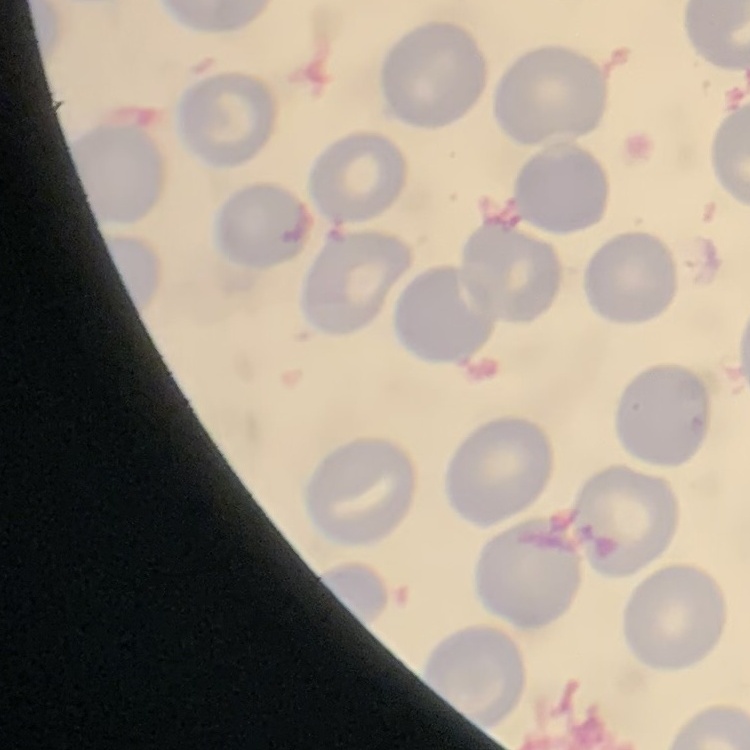

red_blood_cell_morphology: no rouleaux formation
image_type: square crop of a larger photomicrograph
stain: Field's or Giemsa
preparation: thin blood film